Describe the morphology of the erythrocytes.
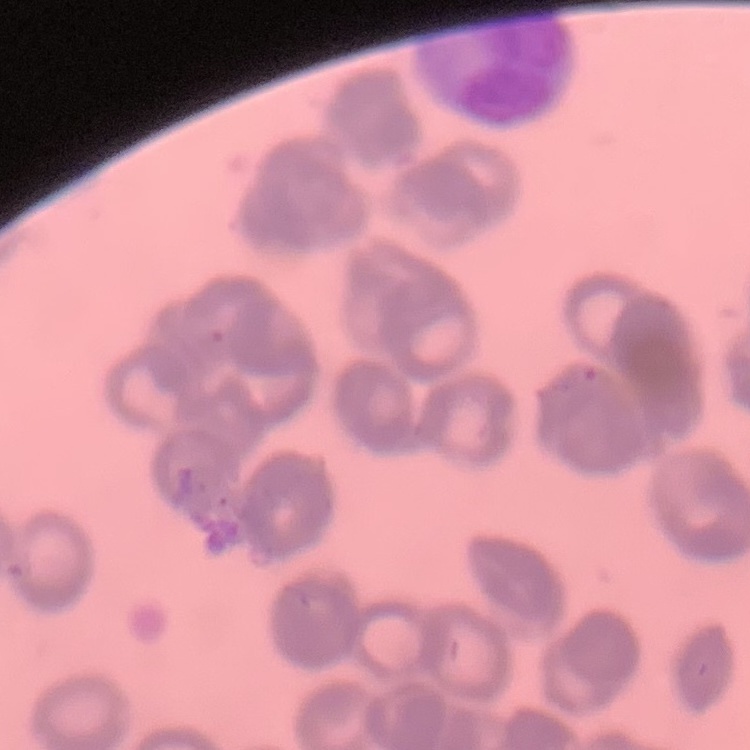

They show rouleaux formation.

preparation = thin peripheral smear
image type = square crop of a larger photomicrograph
stain = Field's or Giemsa